Identify the blood parasite species.
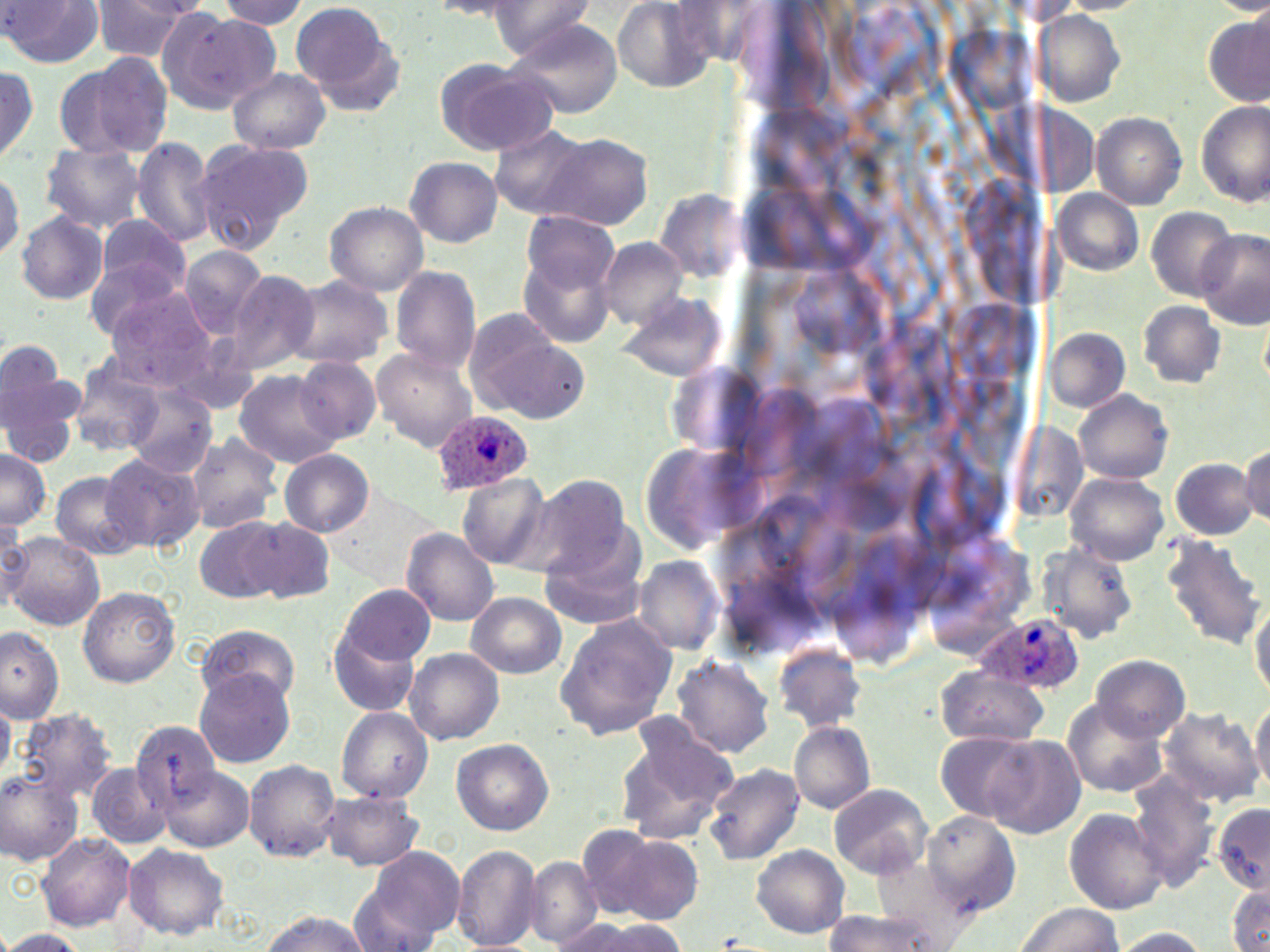
Plasmodium ovale.

stain = May-Grünwald-Giemsa
field of view = single
modality = light microscopy
image size = 1270×952 pixels
Plasmodium ovale-infected red blood cell locations = approximate bounding boxes as (x1, y1, x2, y2) in pixels: (431, 412, 534, 493), (980, 614, 1083, 694)
magnification = 1000x
preparation = thin blood film
uninfected red blood cell locations = approximate bounding boxes as (x1, y1, x2, y2) in pixels: (216, 0, 312, 29), (489, 0, 598, 61), (611, 0, 718, 93), (88, 1, 199, 61), (431, 1, 527, 20), (1, 2, 102, 69), (290, 2, 401, 107), (159, 9, 272, 114), (1031, 9, 1127, 107), (1205, 14, 1269, 106), (506, 16, 624, 119), (58, 53, 173, 159), (436, 59, 559, 156), (0, 60, 39, 165), (227, 68, 331, 154), (1196, 101, 1269, 206), (1092, 112, 1186, 210), (490, 125, 592, 217), (535, 132, 654, 231), (132, 137, 216, 249), (194, 138, 314, 253), (38, 142, 146, 234), (405, 155, 502, 247), (0, 169, 22, 261), (655, 188, 747, 280), (1054, 189, 1143, 275), (324, 201, 429, 297), (1146, 207, 1237, 301), (16, 211, 109, 304), (521, 212, 618, 297), (96, 215, 193, 303), (1199, 231, 1269, 327), (518, 234, 620, 350), (597, 236, 691, 328), (179, 246, 270, 337), (84, 258, 195, 346), (390, 266, 481, 373), (228, 271, 320, 373), (285, 276, 392, 370), (102, 285, 222, 389), (614, 289, 729, 383), (1137, 301, 1225, 388), (468, 317, 584, 422), (1046, 329, 1129, 411), (0, 339, 76, 446), (372, 347, 478, 452), (68, 354, 167, 457), (294, 356, 382, 446), (233, 370, 343, 469), (124, 385, 218, 478), (1075, 390, 1173, 484), (184, 433, 284, 534), (1241, 444, 1270, 525), (0, 448, 53, 529), (279, 450, 374, 537), (100, 452, 202, 551), (1170, 458, 1259, 538), (50, 470, 143, 560), (1067, 473, 1171, 564), (457, 474, 551, 568), (523, 474, 633, 579), (327, 491, 443, 584), (0, 515, 30, 608), (243, 517, 334, 604), (195, 518, 282, 601), (400, 528, 500, 626), (541, 532, 651, 628), (5, 533, 103, 630), (1160, 535, 1265, 652), (1041, 542, 1138, 642), (632, 556, 724, 656), (338, 582, 435, 666), (76, 586, 181, 687), (466, 592, 568, 679), (1251, 599, 1270, 701), (554, 613, 675, 742), (325, 621, 419, 718), (1, 624, 64, 722), (198, 628, 301, 708), (774, 642, 867, 731), (404, 647, 504, 745), (671, 654, 775, 757), (1090, 654, 1191, 742), (934, 667, 1048, 747), (193, 669, 297, 769), (1250, 694, 1270, 795), (0, 697, 15, 782), (1065, 701, 1169, 797), (1154, 705, 1262, 809), (336, 707, 433, 803), (16, 708, 118, 807), (789, 722, 876, 814), (131, 723, 222, 809), (614, 723, 736, 847), (935, 730, 1040, 822), (983, 736, 1085, 837), (452, 739, 553, 834), (244, 760, 341, 862), (86, 762, 172, 849), (704, 763, 804, 865), (161, 766, 253, 851), (0, 769, 83, 865), (1127, 776, 1215, 889), (829, 783, 931, 878), (320, 791, 424, 871), (1212, 803, 1270, 893), (1063, 808, 1170, 914), (923, 811, 1021, 918), (600, 830, 706, 922), (36, 832, 135, 931), (123, 843, 229, 939), (452, 845, 540, 951), (751, 845, 849, 939), (354, 847, 464, 945), (526, 856, 602, 947), (1228, 887, 1270, 951), (1016, 902, 1122, 952), (260, 909, 373, 951), (819, 913, 945, 950), (557, 919, 685, 952), (1113, 927, 1209, 951), (0, 928, 86, 951)